Report the malaria status of this cell.
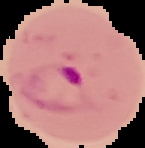
Parasitized.

Summary:
  - Image size: 145×148 pixels
  - Image type: segmented cell region with the area outside set to black
  - Preparation: thin blood film